Assess this cell for malaria.
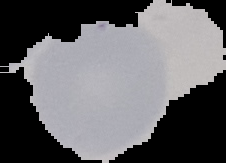

Uninfected.

Image is 226×163 pixels. From a thin blood film. Cell region segmented out of the field of view; the surrounding area is masked to black.